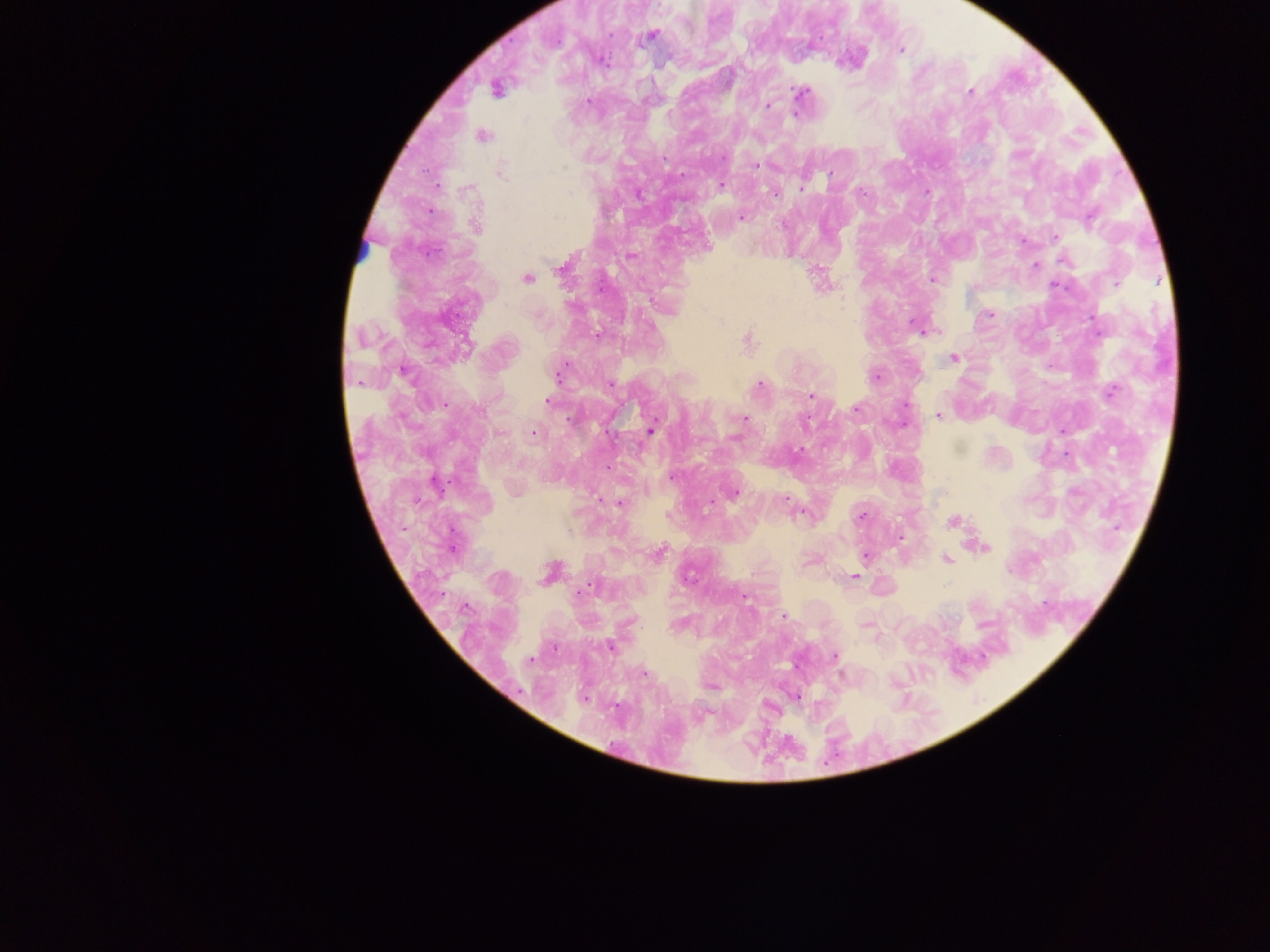

Approximate centers as [x, y] in pixels. Malaria parasite locations: [650, 36], [901, 50], [853, 57], [497, 89], [971, 91], [801, 92], [766, 106], [795, 113], [482, 135], [756, 166], [500, 171], [719, 184], [436, 186], [801, 188], [773, 192], [926, 192], [740, 216], [475, 226], [1055, 237], [1022, 241], [705, 246], [1065, 259], [1035, 265], [562, 267], [526, 278], [932, 279], [1116, 283], [989, 314], [918, 326], [598, 335], [747, 341], [953, 358], [559, 373], [875, 376], [758, 385], [1109, 392], [812, 395], [548, 400], [855, 407], [939, 415], [744, 419], [650, 431], [534, 432], [672, 477], [515, 491], [731, 493], [786, 498], [711, 501], [619, 502], [803, 512], [862, 517], [953, 522], [983, 546], [658, 553], [865, 557], [947, 559], [550, 573], [853, 576], [743, 597], [783, 616], [866, 624], [610, 646], [835, 656], [709, 686], [795, 695]. Leukocyte locations: [367, 249]. Photographed through a microscope with a mobile-phone camera. One field of view. Collected in Ghana. Image is 1270×952 pixels. Thick blood smear.